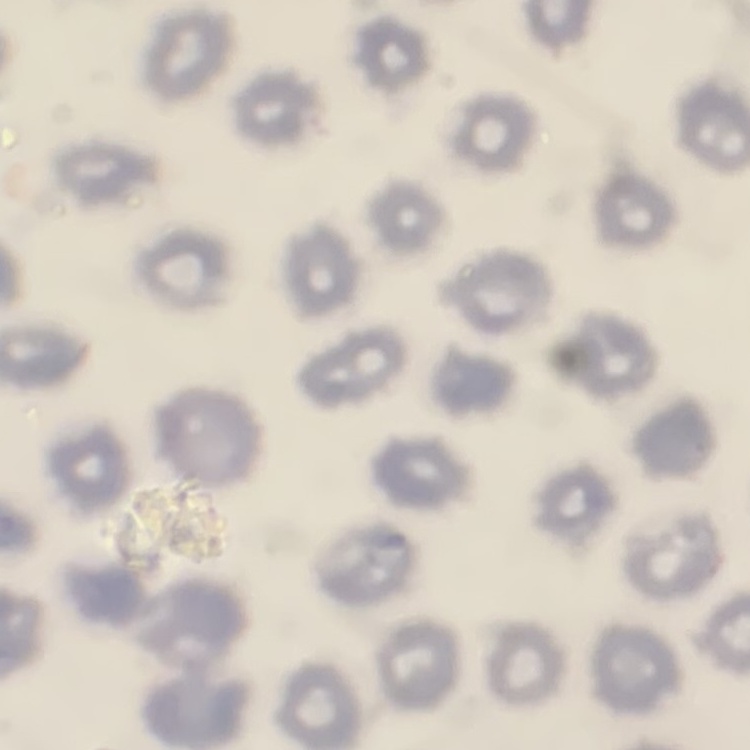
erythrocyte morphology = no rouleaux formation
image type = square crop of a larger photomicrograph
stain = Field's or Giemsa
preparation = thin peripheral smear